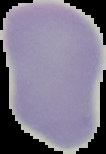
Cell region segmented out of the field of view; the surrounding area is masked to black. Image is 106×154 pixels. Result: negative for Plasmodium parasites. From a thin blood film.